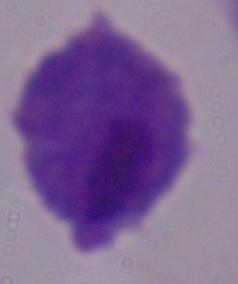
Summary:
  - Identification: trichomonad
  - Modality: micrograph
  - Magnification: 1000x